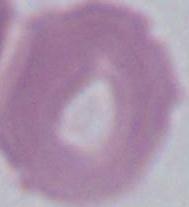

magnification = 1000x
identification = erythrocyte
modality = micrograph